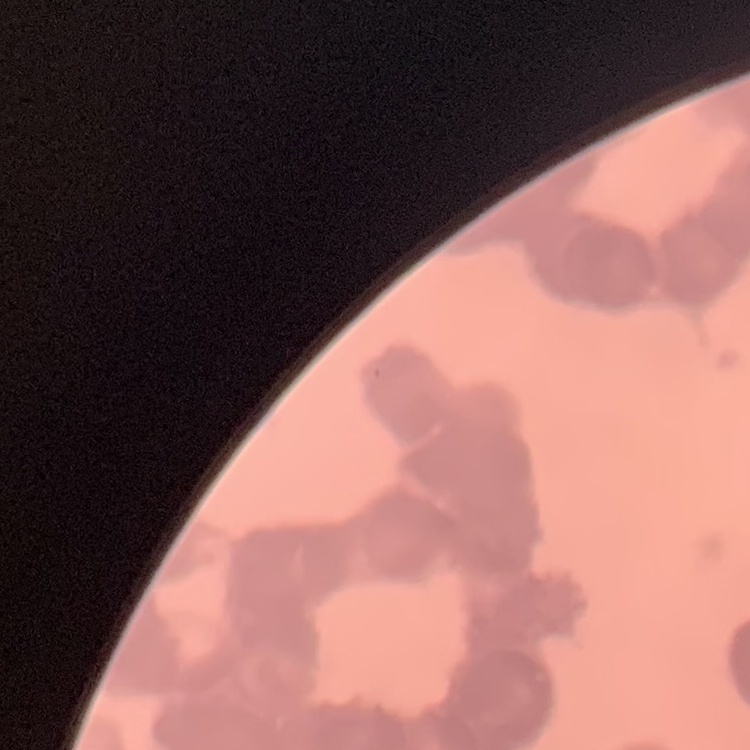 The red blood cells exhibit rouleaux formation. One tile cut from a larger photomicrograph. Stained with either Field's or Giemsa. Thin blood smear.